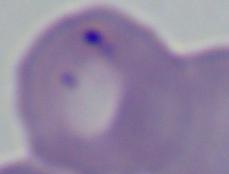 Micrograph. A Babesia parasite is shown. Captured at 1000x magnification.